Classify this cell by malaria status.
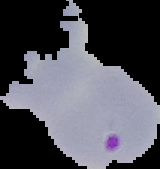
It is parasitized.

Image is 160×169 pixels. From a thin blood film. The area outside the segmented cell region is set to black.